Locate every blood parasite and identify its species.
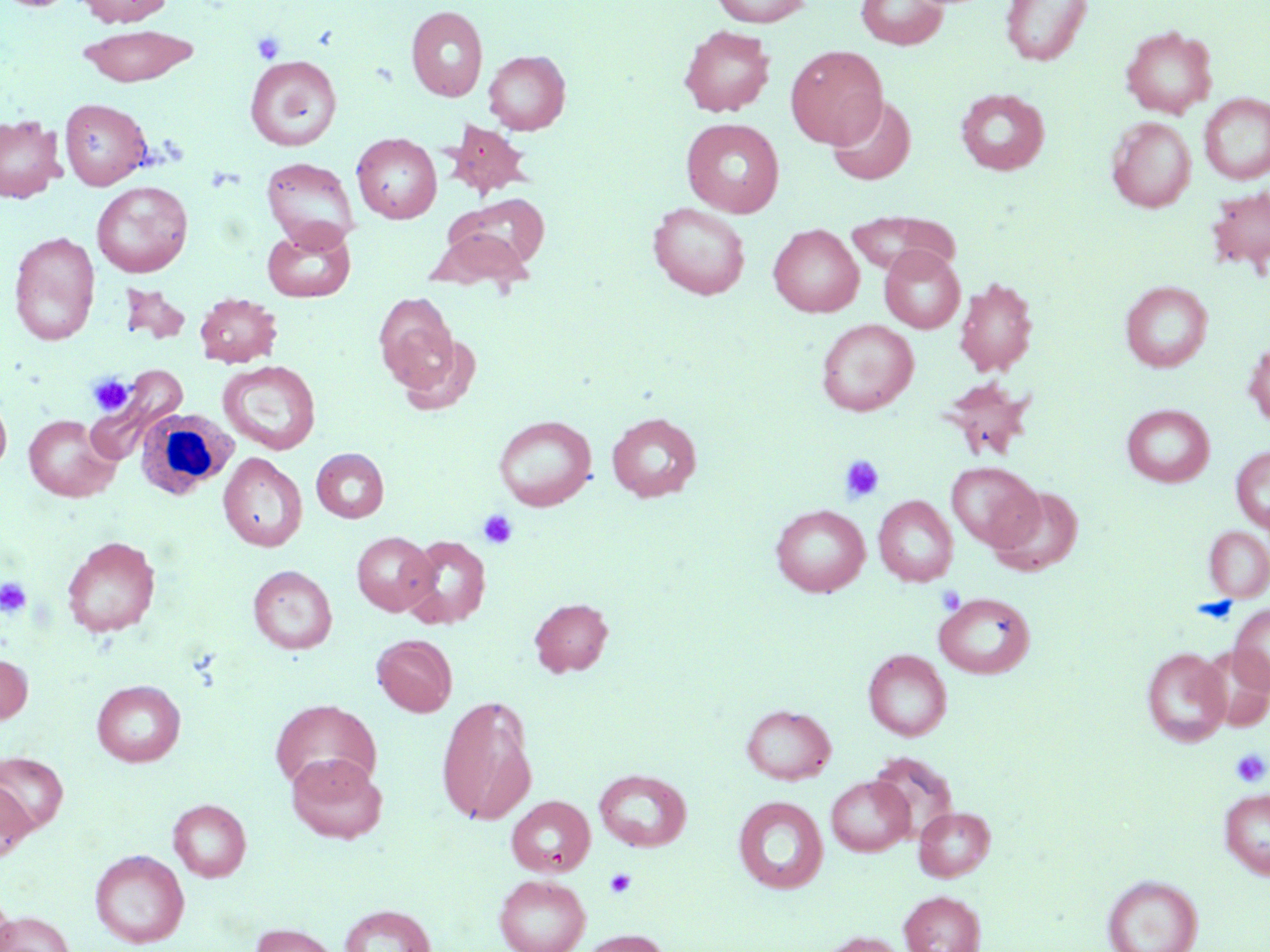
No blood parasites seen.

slide-level diagnosis = no evidence of blood parasites
stain = May-Grünwald-Giemsa
white blood cell locations = approximate bounding boxes as (x1,y1)-(x2,y2) corner pairs in pixels: (135,408)-(241,502)
uninfected red blood cell locations = approximate bounding boxes as (x1,y1)-(x2,y2) corner pairs in pixels: (3,0)-(76,11), (75,0)-(173,27), (711,0)-(812,27), (856,0)-(947,49), (1001,0)-(1092,66), (406,5)-(488,101), (79,24)-(199,88), (679,25)-(775,117), (1120,25)-(1217,118), (785,45)-(888,149), (483,49)-(570,134), (245,55)-(343,151), (956,88)-(1050,175), (1199,93)-(1270,185), (826,95)-(917,186), (59,98)-(152,190), (0,114)-(65,202), (1107,116)-(1195,212), (681,118)-(785,217), (444,121)-(535,199), (352,133)-(441,223), (262,156)-(359,250), (91,181)-(193,277), (1206,186)-(1270,276), (453,193)-(551,273), (648,202)-(751,300), (845,210)-(961,277), (262,223)-(355,303), (769,224)-(863,317), (429,227)-(536,292), (9,231)-(100,345), (880,246)-(965,333), (954,276)-(1038,377), (1120,281)-(1213,372), (195,292)-(282,367), (374,293)-(458,389), (816,318)-(918,416), (394,332)-(482,414), (1244,339)-(1270,428), (219,360)-(321,454), (97,364)-(188,447), (941,379)-(1035,459), (0,393)-(12,476), (1122,404)-(1214,487), (607,412)-(702,502), (23,414)-(120,501), (493,415)-(596,511), (1231,446)-(1270,532), (311,448)-(389,523), (219,453)-(306,551), (946,462)-(1042,551), (988,485)-(1084,576), (874,496)-(958,586), (771,505)-(870,597), (1203,526)-(1270,602), (352,532)-(437,616), (402,535)-(492,628), (61,536)-(160,637), (248,565)-(337,653), (934,592)-(1035,679), (529,598)-(614,677), (1229,604)-(1270,693), (372,635)-(457,716), (1200,646)-(1270,732), (1141,647)-(1230,747), (863,649)-(952,740), (0,654)-(32,724), (92,680)-(186,766), (437,696)-(537,826), (270,699)-(380,793), (741,704)-(836,784), (0,752)-(69,834), (286,753)-(386,843), (594,769)-(692,851), (826,775)-(913,856), (0,778)-(35,862), (1219,788)-(1270,880), (506,796)-(595,877), (733,796)-(828,894), (169,799)-(251,881), (914,806)-(996,881), (90,849)-(189,947), (494,874)-(590,952), (1103,874)-(1203,952), (0,889)-(15,951), (899,890)-(986,952), (339,904)-(436,952), (1,912)-(75,952), (249,923)-(342,952), (574,929)-(671,952), (815,931)-(909,952)
image size = 1270×952 pixels
modality = light microscopy
preparation = thin blood smear
platelet locations = approximate bounding boxes as (x1,y1)-(x2,y2) corner pairs in pixels: (252,31)-(286,64), (87,373)-(136,416), (838,454)-(884,503), (478,510)-(517,549), (0,578)-(32,617), (936,585)-(965,614), (1231,750)-(1269,788), (605,869)-(636,898)
field of view = single
magnification = 1000x